State the preparation type.
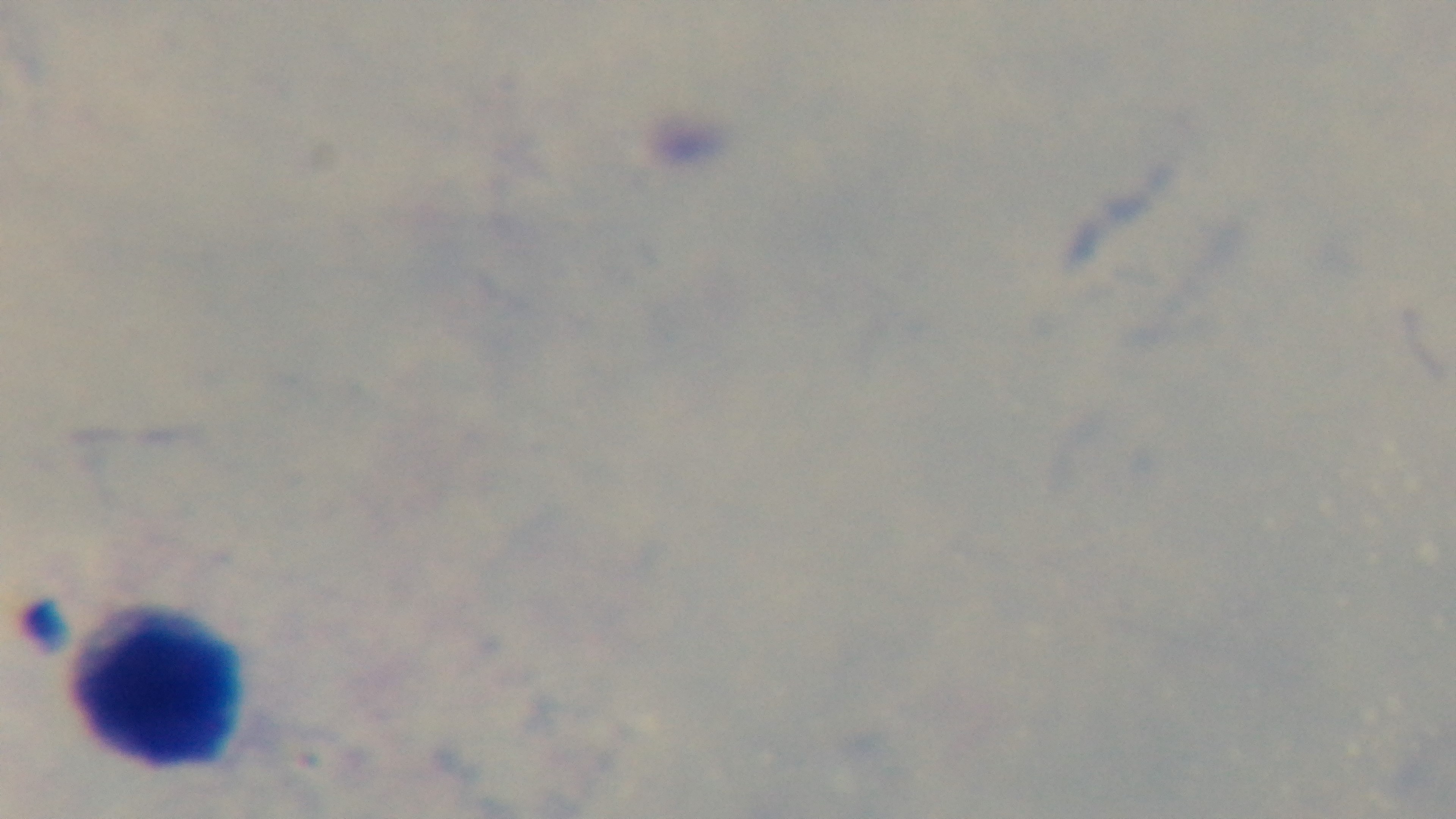

It is a thick blood film.

Summary:
  - Malaria status: negative
  - Field of view: one from the slide
  - Capture: mounted 4K digital camera
  - Modality: light microscopy
  - Stain: Giemsa
  - Objective: 100x oil immersion